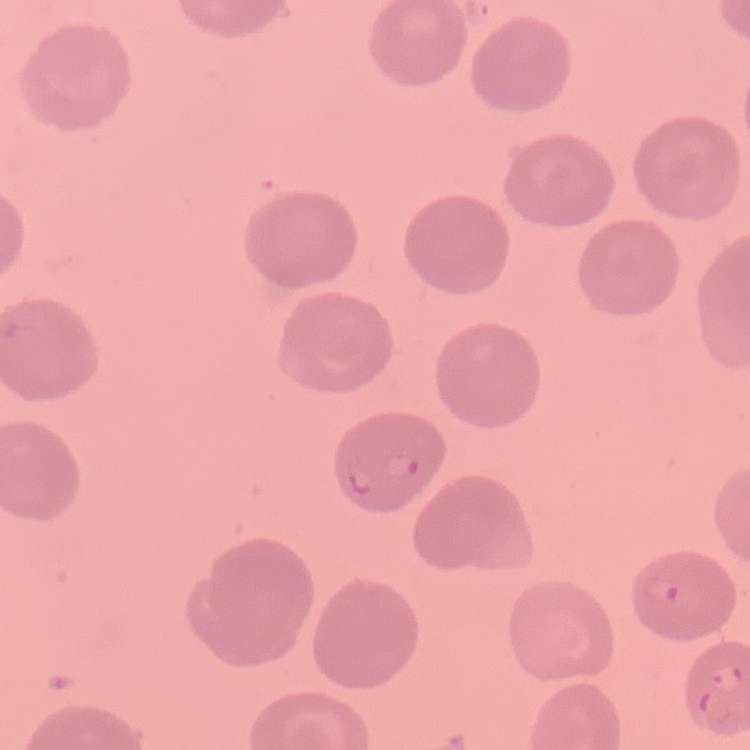
Summary:
  - Red blood cell morphology: no rouleaux formation
  - Stain: Field's or Giemsa
  - Preparation: thin blood film
  - Image type: square crop of a larger photomicrograph